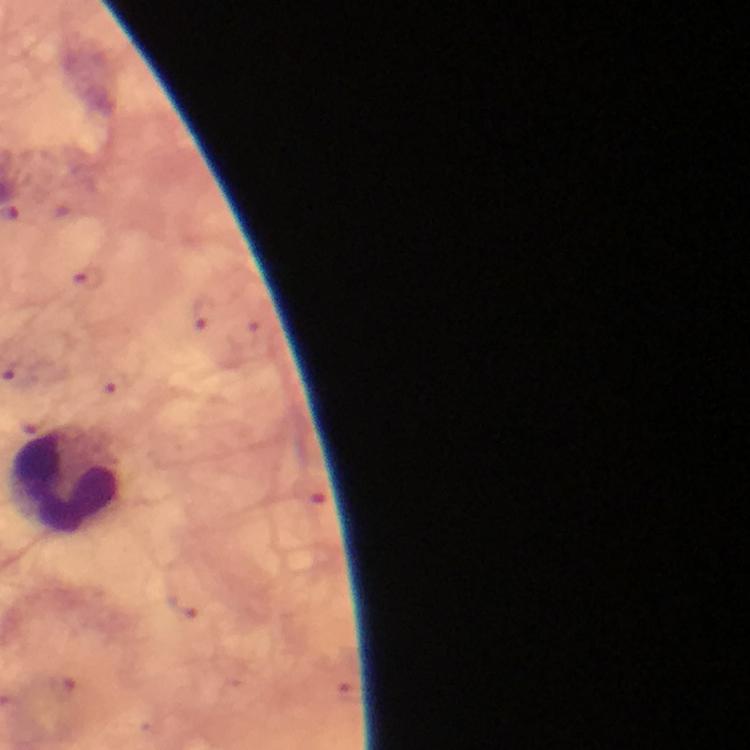 Approximate object centers, in pixels from the top-left corner. Leukocyte locations: (x=69, y=481). Thick blood film. At 100x magnification. Plasmodium parasites: none detected. Smartphone photograph taken through a microscope. Giemsa stain. Cropped region of a single field of view. Image is 750×750 pixels. Immersion oil applied. From a diagnostic examination for malaria.